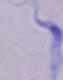 Captured at 1000x magnification. A trypanosome is seen. Photomicrograph.